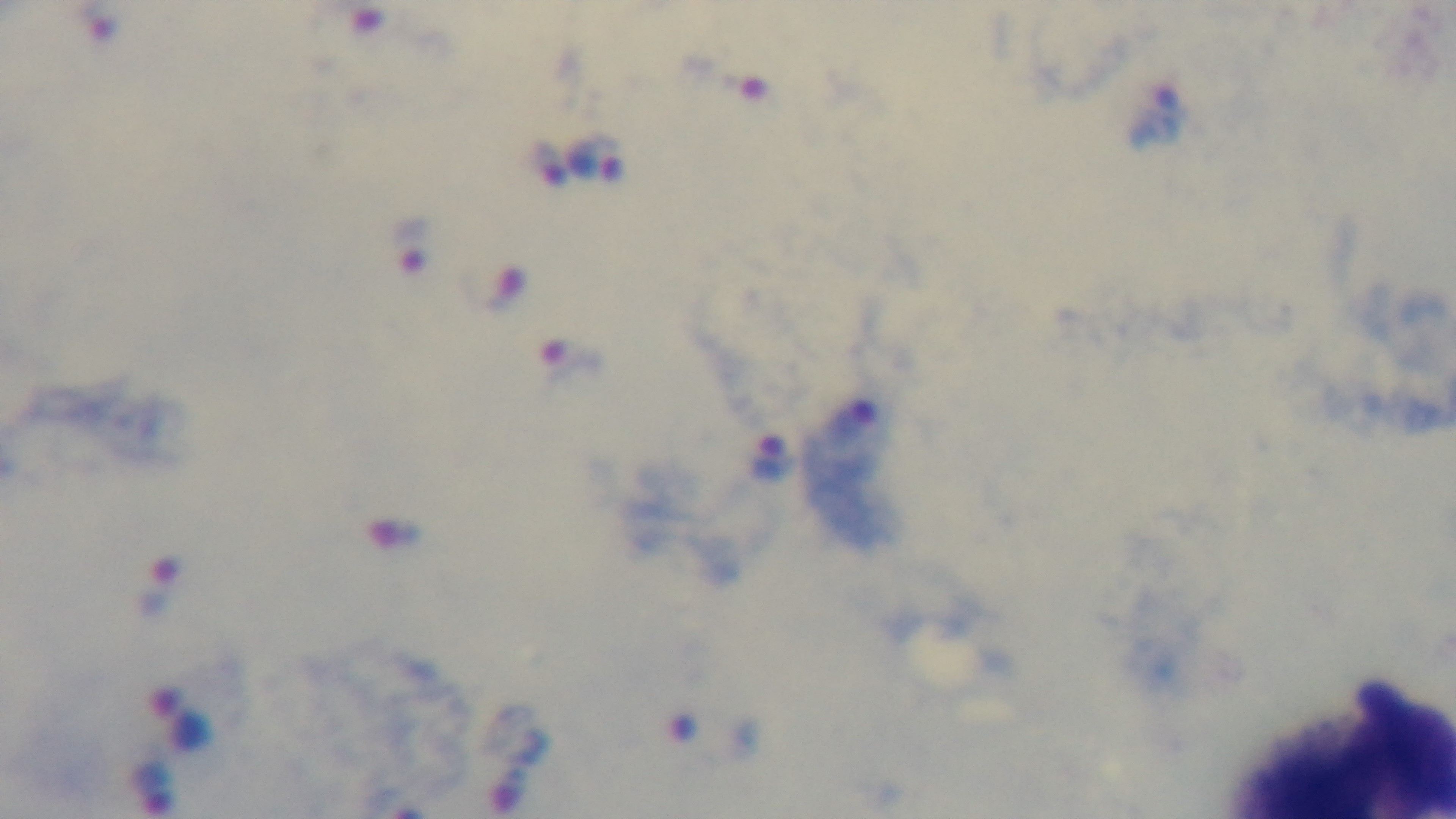

malaria status = infected
stain = Giemsa
modality = light microscopy
objective = 100x oil immersion
field of view = single
preparation = thick blood film
capture = mounted 4K digital camera